Locate the red blood cells and classify each one as Plasmodium falciparum-infected, uninfected, or of indeterminate infection status.
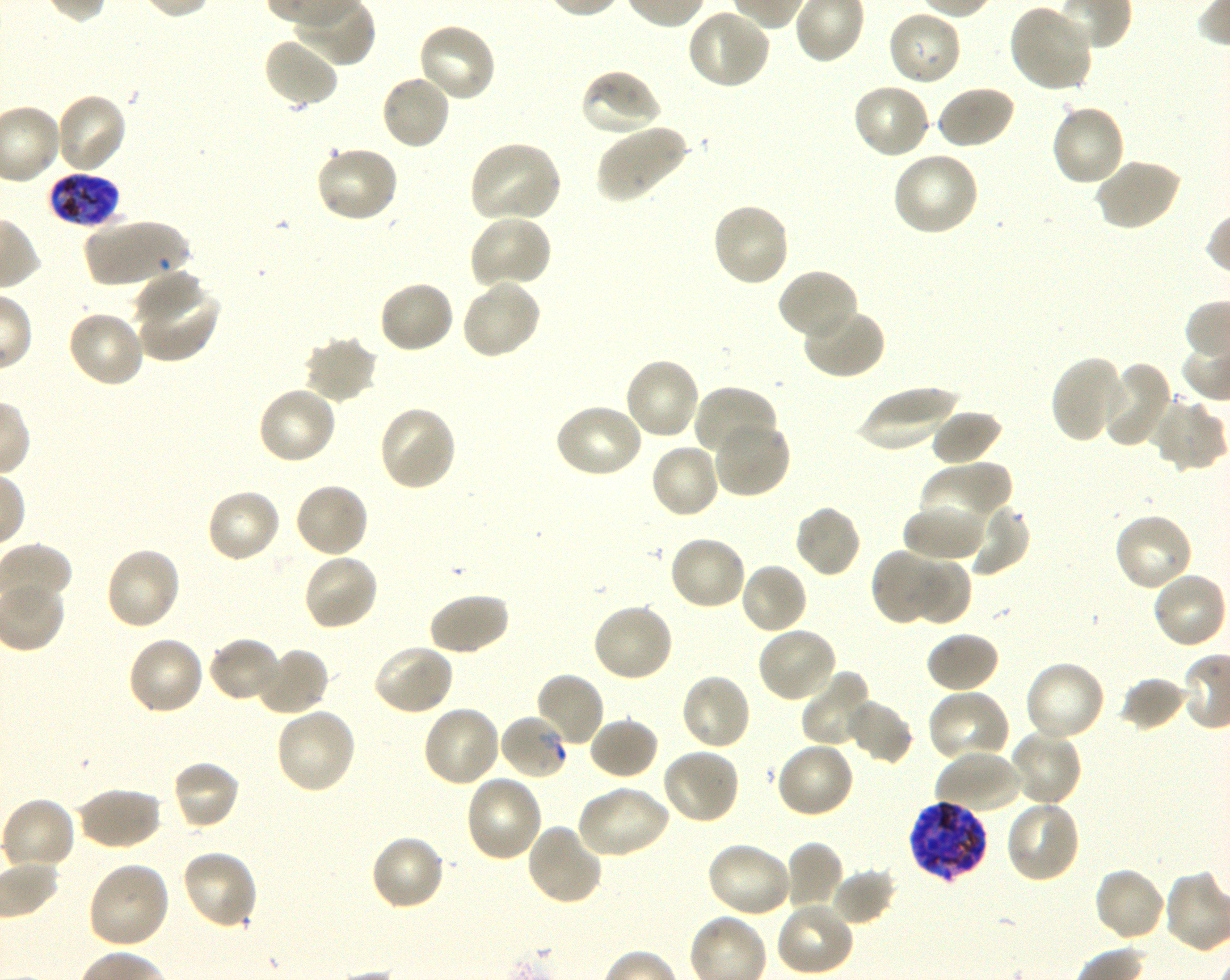
Approximate bounding rectangles given as corner coordinates in pixels from the top-left. Not every red blood cell is marked. A life-cycle stage — or a range of stages, where the recorded stages span more than one — follows each staged infected red blood cell.
Infected red blood cells: (x1=45, y1=172, x2=120, y2=227) late trophozoite to late schizont; (x1=908, y1=800, x2=988, y2=881) late trophozoite to late schizont.
Red blood cells of indeterminate infection status: (x1=498, y1=713, x2=569, y2=781).
Uninfected red blood cells: (x1=1008, y1=4, x2=1093, y2=93), (x1=687, y1=8, x2=771, y2=90), (x1=887, y1=8, x2=963, y2=87), (x1=415, y1=22, x2=497, y2=104), (x1=261, y1=35, x2=340, y2=110), (x1=579, y1=67, x2=663, y2=138), (x1=379, y1=73, x2=453, y2=151), (x1=852, y1=83, x2=932, y2=160), (x1=934, y1=84, x2=1016, y2=150), (x1=54, y1=92, x2=129, y2=174), (x1=1049, y1=103, x2=1126, y2=188), (x1=595, y1=123, x2=690, y2=203), (x1=467, y1=139, x2=564, y2=223), (x1=314, y1=144, x2=400, y2=224), (x1=891, y1=150, x2=979, y2=237), (x1=1094, y1=158, x2=1183, y2=232), (x1=710, y1=201, x2=791, y2=288), (x1=468, y1=214, x2=554, y2=290), (x1=83, y1=219, x2=193, y2=287), (x1=134, y1=268, x2=205, y2=323), (x1=776, y1=268, x2=859, y2=342), (x1=378, y1=279, x2=456, y2=355), (x1=461, y1=279, x2=542, y2=359), (x1=135, y1=280, x2=220, y2=363), (x1=801, y1=306, x2=886, y2=380), (x1=66, y1=308, x2=146, y2=389), (x1=302, y1=334, x2=379, y2=404), (x1=1049, y1=355, x2=1126, y2=443), (x1=623, y1=356, x2=701, y2=441), (x1=1094, y1=361, x2=1174, y2=448), (x1=692, y1=384, x2=780, y2=463), (x1=853, y1=385, x2=961, y2=452), (x1=256, y1=386, x2=339, y2=466), (x1=1151, y1=398, x2=1226, y2=472), (x1=554, y1=403, x2=644, y2=480), (x1=377, y1=405, x2=457, y2=493), (x1=930, y1=410, x2=1004, y2=466), (x1=710, y1=420, x2=791, y2=500), (x1=649, y1=443, x2=721, y2=520), (x1=919, y1=461, x2=1012, y2=536), (x1=293, y1=481, x2=370, y2=559), (x1=205, y1=487, x2=282, y2=564), (x1=964, y1=503, x2=1032, y2=578), (x1=793, y1=504, x2=863, y2=579), (x1=904, y1=504, x2=986, y2=562), (x1=1112, y1=512, x2=1194, y2=593), (x1=667, y1=534, x2=748, y2=612), (x1=104, y1=546, x2=181, y2=632), (x1=870, y1=547, x2=949, y2=626), (x1=302, y1=553, x2=379, y2=632), (x1=910, y1=558, x2=972, y2=626), (x1=738, y1=562, x2=808, y2=636), (x1=1151, y1=572, x2=1228, y2=650), (x1=427, y1=592, x2=511, y2=658), (x1=590, y1=602, x2=674, y2=683), (x1=755, y1=627, x2=839, y2=704), (x1=925, y1=631, x2=1001, y2=694), (x1=127, y1=635, x2=206, y2=716), (x1=207, y1=637, x2=283, y2=703), (x1=371, y1=642, x2=455, y2=716), (x1=255, y1=646, x2=330, y2=717), (x1=1023, y1=660, x2=1106, y2=742), (x1=800, y1=670, x2=874, y2=748), (x1=533, y1=671, x2=605, y2=748), (x1=679, y1=672, x2=753, y2=751), (x1=1120, y1=676, x2=1188, y2=731), (x1=927, y1=688, x2=1012, y2=764), (x1=845, y1=698, x2=914, y2=765), (x1=421, y1=705, x2=502, y2=788), (x1=274, y1=706, x2=358, y2=794), (x1=588, y1=717, x2=660, y2=781), (x1=1009, y1=728, x2=1083, y2=808), (x1=775, y1=741, x2=856, y2=819), (x1=661, y1=748, x2=741, y2=825), (x1=934, y1=748, x2=1022, y2=815), (x1=171, y1=759, x2=241, y2=832), (x1=464, y1=773, x2=544, y2=862), (x1=576, y1=784, x2=671, y2=860), (x1=75, y1=786, x2=162, y2=851), (x1=1, y1=796, x2=76, y2=872), (x1=1005, y1=799, x2=1082, y2=884), (x1=525, y1=823, x2=605, y2=907), (x1=368, y1=834, x2=446, y2=912), (x1=784, y1=841, x2=843, y2=911), (x1=705, y1=842, x2=794, y2=919), (x1=180, y1=847, x2=260, y2=929), (x1=87, y1=861, x2=171, y2=949), (x1=1093, y1=866, x2=1167, y2=942), (x1=830, y1=868, x2=897, y2=926), (x1=775, y1=900, x2=855, y2=976).

Blood group of the donor: O+. Thin blood film. Giemsa-stained preparation. Image is 1230×980 pixels. Oil immersion, 100x objective (numerical aperture 1.30). Single field of view. Plasmodium falciparum strain 3D7 maintained in shaking in-vitro culture.